Name the cell type shown.
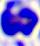

A leukocyte.

Micrograph. Captured at 400x magnification.